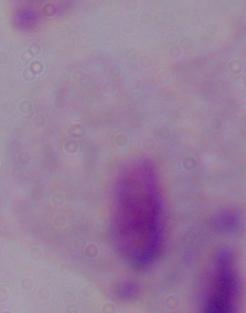 A trichomonad is shown. 1000x magnification. Photomicrograph.